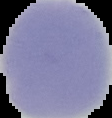

Summary:
  - Image type: cell region segmented out of the field of view; surrounding area masked to black
  - Preparation: thin blood film
  - Image size: 112×118 pixels
  - Result: no malaria parasites seen